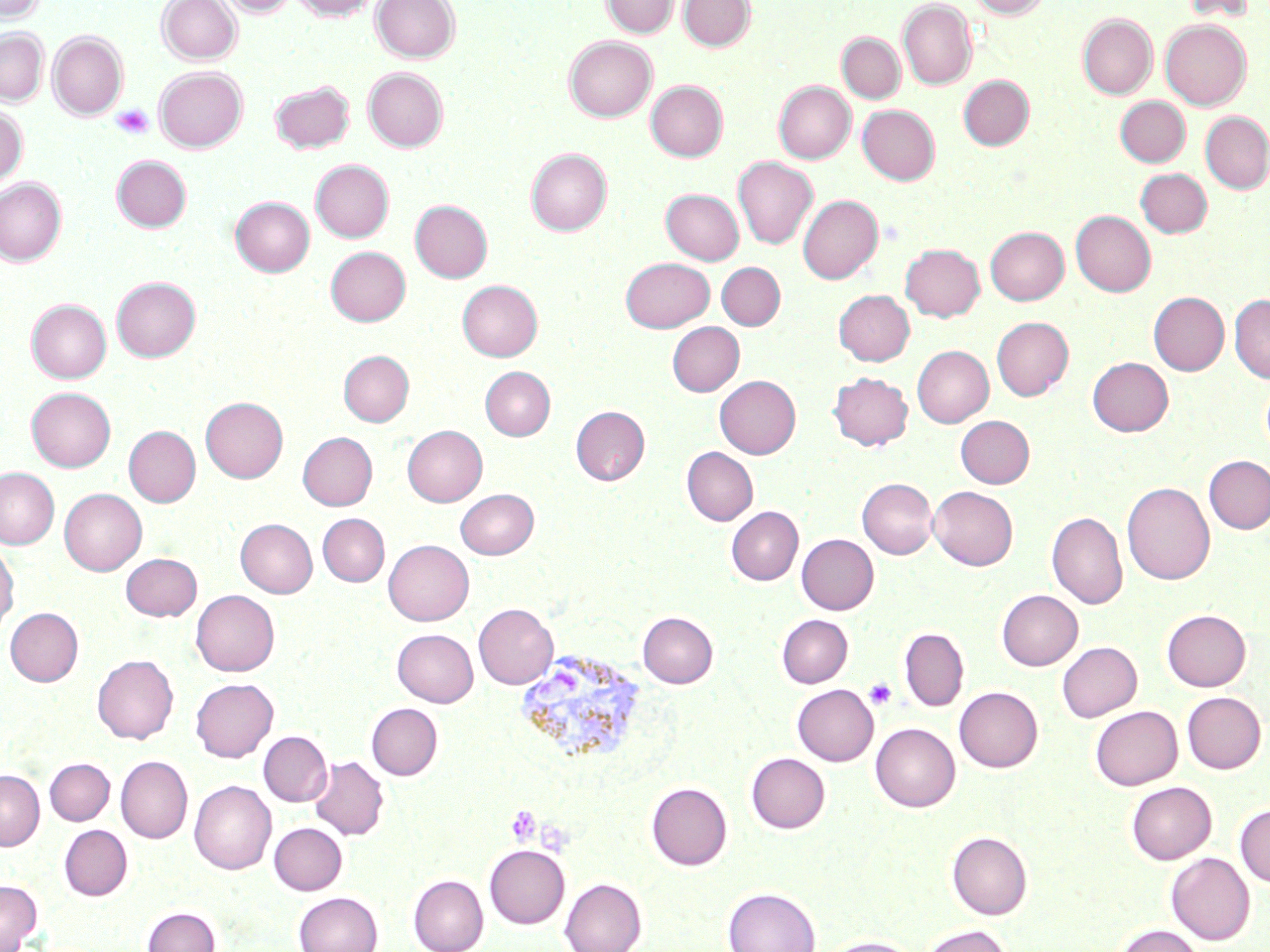 Approximate bounding boxes as named x1/y1/x2/y2 corners in pixels. Plasmodium vivax-infected red blood cell locations: (x1=518, y1=654, x2=644, y2=771). Platelet locations: (x1=113, y1=104, x2=154, y2=140), (x1=863, y1=678, x2=898, y2=710), (x1=505, y1=805, x2=542, y2=845). Uninfected red blood cell locations: (x1=0, y1=0, x2=44, y2=23), (x1=157, y1=0, x2=241, y2=64), (x1=219, y1=0, x2=296, y2=17), (x1=291, y1=0, x2=379, y2=20), (x1=371, y1=0, x2=460, y2=62), (x1=601, y1=0, x2=679, y2=37), (x1=679, y1=0, x2=755, y2=51), (x1=969, y1=0, x2=1049, y2=18), (x1=1182, y1=0, x2=1255, y2=23), (x1=898, y1=1, x2=976, y2=90), (x1=1078, y1=14, x2=1157, y2=98), (x1=1161, y1=19, x2=1251, y2=109), (x1=0, y1=29, x2=48, y2=105), (x1=48, y1=31, x2=128, y2=119), (x1=837, y1=33, x2=905, y2=103), (x1=564, y1=36, x2=657, y2=121), (x1=154, y1=67, x2=247, y2=153), (x1=363, y1=68, x2=448, y2=152), (x1=959, y1=75, x2=1033, y2=149), (x1=270, y1=80, x2=354, y2=152), (x1=646, y1=80, x2=728, y2=161), (x1=774, y1=81, x2=855, y2=163), (x1=1115, y1=96, x2=1190, y2=166), (x1=858, y1=105, x2=939, y2=184), (x1=0, y1=106, x2=27, y2=187), (x1=1200, y1=112, x2=1270, y2=194), (x1=526, y1=148, x2=611, y2=235), (x1=112, y1=155, x2=191, y2=232), (x1=733, y1=157, x2=818, y2=249), (x1=311, y1=160, x2=394, y2=242), (x1=1135, y1=168, x2=1211, y2=237), (x1=0, y1=177, x2=66, y2=265), (x1=661, y1=189, x2=744, y2=264), (x1=798, y1=195, x2=883, y2=283), (x1=230, y1=196, x2=315, y2=276), (x1=410, y1=200, x2=492, y2=282), (x1=1071, y1=210, x2=1156, y2=297), (x1=985, y1=226, x2=1069, y2=304), (x1=900, y1=243, x2=985, y2=321), (x1=326, y1=246, x2=410, y2=325), (x1=620, y1=257, x2=714, y2=332), (x1=716, y1=262, x2=785, y2=330), (x1=112, y1=277, x2=200, y2=362), (x1=457, y1=280, x2=542, y2=360), (x1=834, y1=290, x2=914, y2=366), (x1=1149, y1=292, x2=1229, y2=375), (x1=1230, y1=294, x2=1270, y2=384), (x1=26, y1=299, x2=111, y2=382), (x1=992, y1=317, x2=1073, y2=400), (x1=667, y1=322, x2=744, y2=396), (x1=912, y1=346, x2=993, y2=427), (x1=339, y1=350, x2=414, y2=426), (x1=1088, y1=357, x2=1173, y2=436), (x1=481, y1=367, x2=555, y2=440), (x1=828, y1=372, x2=912, y2=451), (x1=715, y1=375, x2=800, y2=458), (x1=1261, y1=379, x2=1270, y2=457), (x1=27, y1=387, x2=115, y2=471), (x1=201, y1=397, x2=287, y2=482), (x1=571, y1=405, x2=649, y2=485), (x1=956, y1=415, x2=1034, y2=488), (x1=402, y1=425, x2=487, y2=506), (x1=124, y1=426, x2=200, y2=506), (x1=297, y1=432, x2=377, y2=510), (x1=682, y1=447, x2=757, y2=525), (x1=1203, y1=455, x2=1270, y2=534), (x1=0, y1=468, x2=59, y2=549), (x1=858, y1=478, x2=937, y2=558), (x1=1123, y1=481, x2=1215, y2=585), (x1=929, y1=486, x2=1017, y2=570), (x1=456, y1=488, x2=538, y2=558), (x1=60, y1=489, x2=146, y2=575), (x1=726, y1=507, x2=803, y2=585), (x1=1047, y1=511, x2=1128, y2=609), (x1=317, y1=514, x2=389, y2=586), (x1=236, y1=518, x2=317, y2=597), (x1=797, y1=534, x2=878, y2=614), (x1=384, y1=539, x2=473, y2=626), (x1=0, y1=542, x2=19, y2=634), (x1=121, y1=553, x2=202, y2=621), (x1=191, y1=590, x2=279, y2=676), (x1=997, y1=590, x2=1082, y2=670), (x1=474, y1=603, x2=558, y2=689), (x1=5, y1=607, x2=83, y2=686), (x1=1162, y1=609, x2=1251, y2=691), (x1=638, y1=612, x2=718, y2=687), (x1=777, y1=614, x2=852, y2=687), (x1=899, y1=628, x2=969, y2=712), (x1=392, y1=629, x2=478, y2=706), (x1=1057, y1=641, x2=1141, y2=721), (x1=92, y1=655, x2=178, y2=743), (x1=191, y1=678, x2=278, y2=762), (x1=792, y1=684, x2=878, y2=765), (x1=954, y1=686, x2=1043, y2=772), (x1=1182, y1=692, x2=1266, y2=773), (x1=366, y1=703, x2=442, y2=780), (x1=1090, y1=705, x2=1182, y2=790), (x1=870, y1=723, x2=960, y2=811), (x1=259, y1=731, x2=332, y2=806), (x1=746, y1=752, x2=830, y2=833), (x1=116, y1=756, x2=192, y2=843), (x1=310, y1=756, x2=388, y2=840), (x1=45, y1=758, x2=114, y2=824), (x1=0, y1=770, x2=44, y2=849), (x1=189, y1=780, x2=276, y2=875), (x1=1126, y1=781, x2=1216, y2=864), (x1=646, y1=782, x2=732, y2=870), (x1=1235, y1=804, x2=1270, y2=887), (x1=269, y1=822, x2=347, y2=895), (x1=59, y1=825, x2=132, y2=899), (x1=947, y1=830, x2=1032, y2=919), (x1=484, y1=844, x2=569, y2=928), (x1=1166, y1=852, x2=1255, y2=944), (x1=409, y1=875, x2=488, y2=952), (x1=560, y1=878, x2=646, y2=952), (x1=0, y1=880, x2=41, y2=952), (x1=723, y1=886, x2=820, y2=952), (x1=293, y1=891, x2=382, y2=952), (x1=143, y1=905, x2=220, y2=952), (x1=919, y1=924, x2=1013, y2=952), (x1=1115, y1=924, x2=1205, y2=952), (x1=820, y1=935, x2=922, y2=952). Slide-level diagnosis: Plasmodium vivax. Thin blood film. May-Grünwald-Giemsa stain. Image is 1270×952 pixels. Captured at 1000x magnification. One field of a larger specimen. Light microscopy.